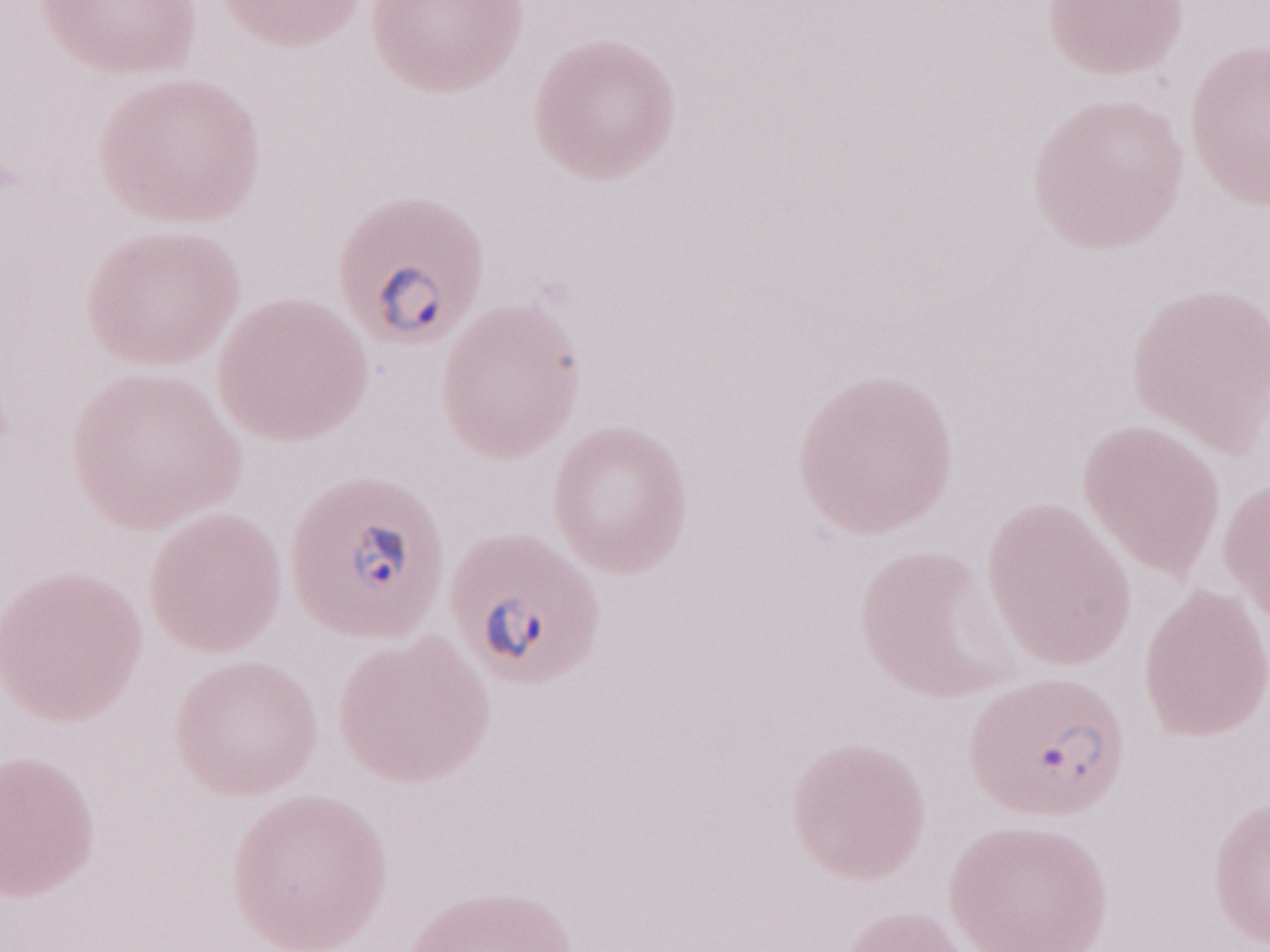 One field of this slide. 1,000x magnification. Image is 1270×952 pixels. May-Grünwald-Giemsa (MGG) stain. Olympus BX43 microscope, Olympus DP73 camera. Malaria diagnosis (patient-level): positive. Thin peripheral-blood smear.